Give the extent of all Plasmodium falciparum-infected red blood cells.
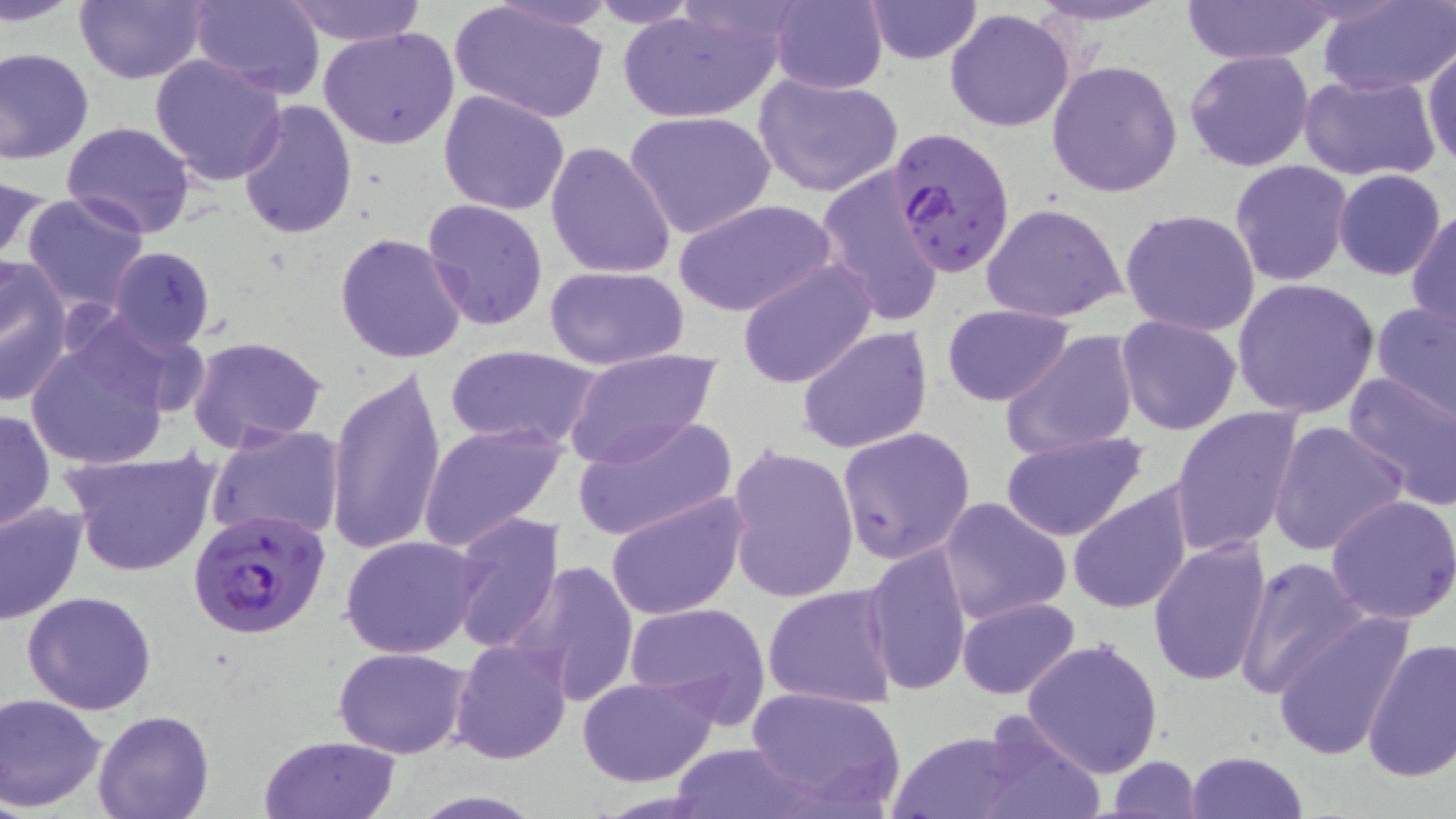
Approximate bounding boxes as (x1, y1, x2, y2) in pixels.
Plasmodium falciparum-infected red blood cells: (889, 125, 1015, 278), (188, 505, 330, 638).

slide-level diagnosis = Plasmodium falciparum
stain = May-Grünwald-Giemsa
magnification = 1000x
modality = optical microscopy
field of view = one of a larger specimen
uninfected red blood cell locations = approximate bounding boxes as (x1, y1, x2, y2) in pixels: (3, 0, 83, 26), (74, 0, 207, 85), (191, 0, 326, 99), (769, 0, 889, 94), (863, 0, 982, 65), (1024, 0, 1175, 27), (1184, 0, 1333, 65), (278, 1, 431, 45), (583, 1, 706, 27), (1317, 1, 1456, 97), (449, 3, 612, 125), (617, 7, 783, 124), (944, 8, 1075, 132), (321, 27, 458, 150), (1422, 43, 1456, 171), (0, 47, 95, 164), (1184, 49, 1315, 172), (150, 53, 289, 186), (1048, 59, 1182, 197), (753, 73, 903, 198), (1299, 74, 1441, 182), (438, 89, 570, 215), (237, 98, 358, 238), (623, 111, 776, 240), (62, 122, 194, 239), (545, 140, 678, 278), (1230, 161, 1352, 286), (815, 168, 947, 326), (1334, 170, 1446, 281), (0, 172, 48, 270), (21, 192, 149, 313), (421, 198, 550, 333), (675, 199, 836, 318), (981, 202, 1127, 324), (1120, 207, 1260, 337), (1408, 207, 1456, 334), (334, 232, 467, 364), (107, 247, 216, 351), (0, 255, 73, 407), (736, 259, 878, 389), (545, 264, 691, 370), (1231, 276, 1380, 419), (1370, 298, 1456, 424), (941, 304, 1073, 405), (1114, 314, 1243, 437), (796, 325, 934, 453), (23, 326, 176, 471), (999, 330, 1141, 461), (187, 335, 327, 454), (445, 346, 601, 453), (562, 348, 721, 469), (328, 366, 449, 554), (1343, 369, 1456, 512), (1169, 406, 1303, 556), (1, 407, 54, 534), (572, 414, 738, 542), (1268, 419, 1408, 557), (418, 422, 566, 552), (205, 423, 346, 544), (837, 426, 976, 563), (1001, 430, 1149, 541), (725, 446, 859, 604), (61, 447, 223, 578), (1067, 481, 1195, 615), (607, 492, 748, 620), (1326, 495, 1456, 625), (938, 496, 1071, 624), (0, 500, 88, 625), (448, 511, 563, 655), (340, 535, 483, 657), (1147, 536, 1273, 691), (862, 543, 972, 698), (1233, 557, 1373, 698), (509, 563, 641, 705), (762, 583, 899, 708), (23, 591, 156, 715), (956, 596, 1081, 699), (623, 601, 772, 729), (1268, 612, 1414, 761), (449, 638, 573, 764), (1022, 638, 1167, 778), (1360, 639, 1456, 782), (334, 645, 473, 759), (576, 675, 719, 787), (745, 686, 905, 812), (0, 694, 108, 812), (93, 708, 215, 819), (967, 711, 1117, 819), (880, 727, 1050, 819), (260, 734, 401, 819), (669, 743, 814, 818), (1185, 750, 1310, 819), (1107, 757, 1201, 817)
image size = 1456×819 pixels
preparation = thin blood smear